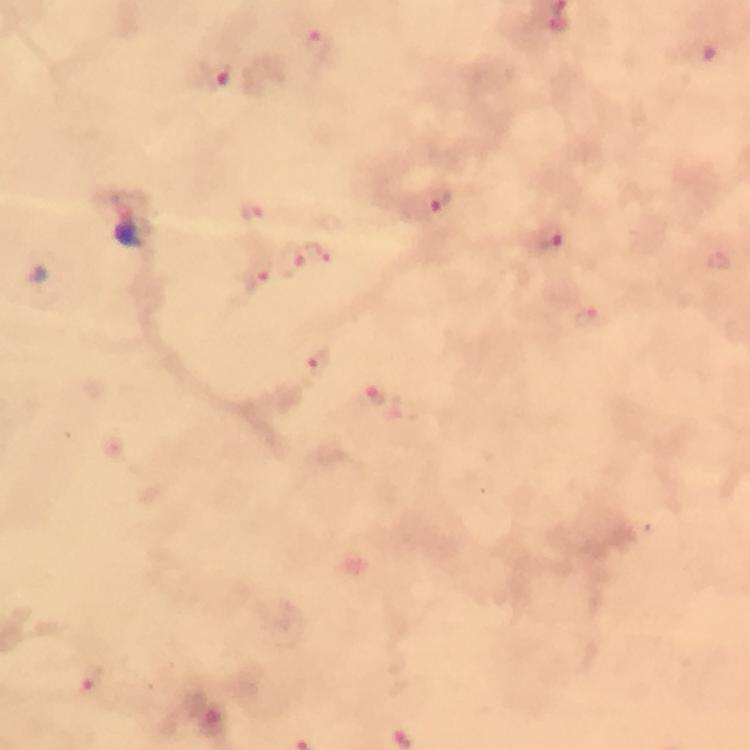

{
  "magnification": "100x",
  "stain": "Giemsa",
  "context": "from a malaria diagnostic workup",
  "capture": "smartphone mounted on the microscope",
  "image_size": "750×750 pixels",
  "immersion_oil": "applied",
  "plasmodium_parasite_locations": "approximate object centers, in pixels from the top-left corner: (x=319, y=363), (x=371, y=395), (x=92, y=684)",
  "cropped_from": "a single field of view",
  "preparation": "thick blood smear"
}